Locate every uninfected red blood cell.
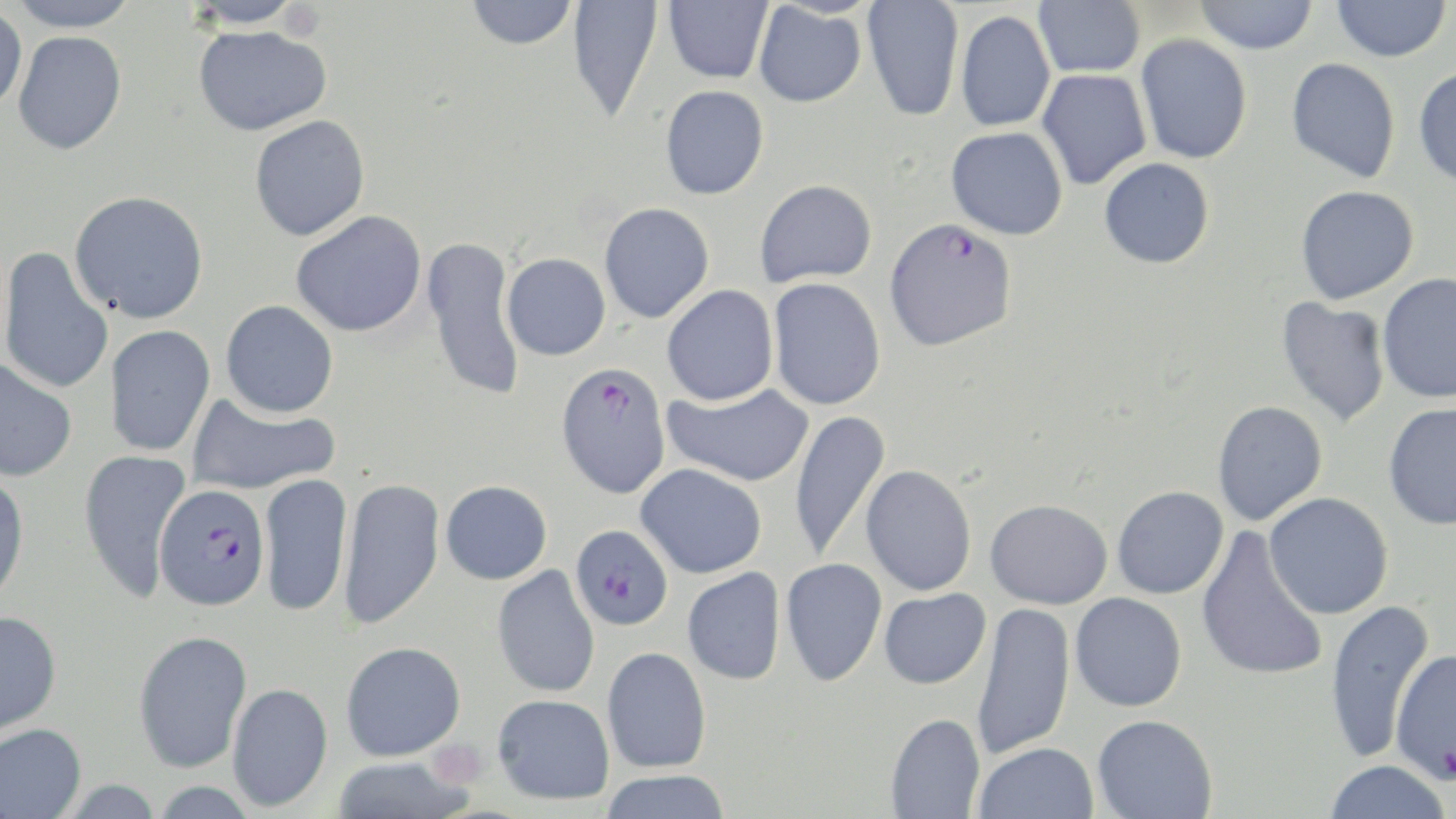
Approximate bounding boxes as (x1,y1)-(x2,y2) corner pairs in pixels.
Uninfected red blood cells: (5,0)-(140,32), (182,0)-(306,29), (464,0)-(578,50), (568,0)-(664,124), (663,0)-(773,84), (862,0)-(965,122), (1033,0)-(1145,78), (1193,0)-(1319,54), (1332,0)-(1451,62), (753,3)-(867,108), (0,4)-(27,115), (955,9)-(1056,132), (192,24)-(331,136), (12,31)-(127,155), (1135,34)-(1253,164), (1286,57)-(1400,183), (1413,66)-(1456,189), (1036,69)-(1152,191), (660,85)-(769,200), (249,115)-(370,241), (946,126)-(1068,240), (1099,157)-(1215,269), (754,178)-(877,287), (1295,185)-(1419,303), (69,190)-(209,323), (598,202)-(715,324), (291,210)-(427,337), (423,235)-(526,404), (0,246)-(114,397), (502,253)-(611,361), (1376,273)-(1456,403), (767,277)-(886,410), (661,284)-(779,406), (1275,296)-(1391,428), (220,300)-(339,418), (104,325)-(216,457), (0,358)-(77,482), (662,383)-(815,487), (187,392)-(340,496), (1212,400)-(1328,526), (1383,402)-(1456,530), (790,409)-(891,564), (78,448)-(192,603), (635,463)-(768,579), (860,464)-(978,596), (0,472)-(30,609), (258,472)-(352,618), (337,476)-(444,631), (440,480)-(552,584), (1111,485)-(1229,599), (1264,492)-(1393,619), (985,499)-(1113,609), (1195,527)-(1329,683), (780,557)-(887,687), (492,565)-(600,698), (682,567)-(786,685), (878,588)-(991,689), (1070,592)-(1187,712), (1325,598)-(1435,762), (971,601)-(1076,760), (0,610)-(62,739), (133,629)-(253,773), (340,641)-(466,761), (1389,646)-(1456,784), (601,647)-(712,773), (227,682)-(333,812), (492,693)-(615,805), (885,712)-(985,818), (1092,714)-(1218,819), (0,724)-(87,818), (974,741)-(1098,819), (331,756)-(474,818), (1324,760)-(1451,819), (597,770)-(732,819).

Summary:
  - Plasmodium falciparum-infected red blood cell locations: (884,217)-(1018,351), (555,360)-(671,499), (154,484)-(271,610), (570,523)-(674,631)
  - Slide-level diagnosis: Plasmodium falciparum
  - Field of view: one of a larger specimen
  - Preparation: thin blood film
  - Modality: light microscopy
  - Magnification: 1000x
  - Stain: May-Grünwald-Giemsa
  - Image size: 1456×819 pixels